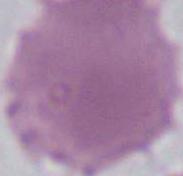

magnification = 1000x
modality = photomicrograph
identification = red blood cell